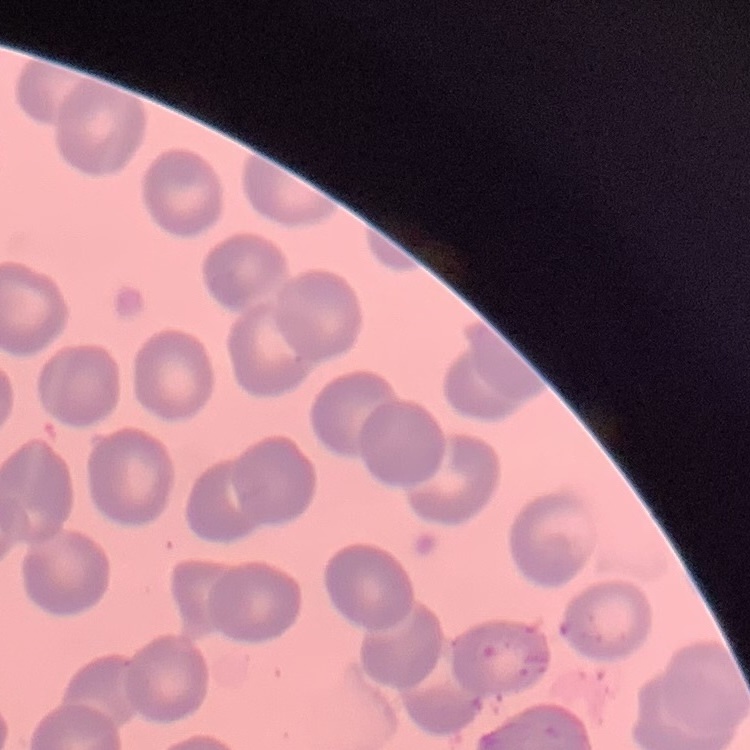
{
  "erythrocyte_morphology": "no rouleaux formation",
  "image_type": "one tile cut from a larger photomicrograph",
  "preparation": "thin blood smear",
  "stain": "Field's or Giemsa"
}